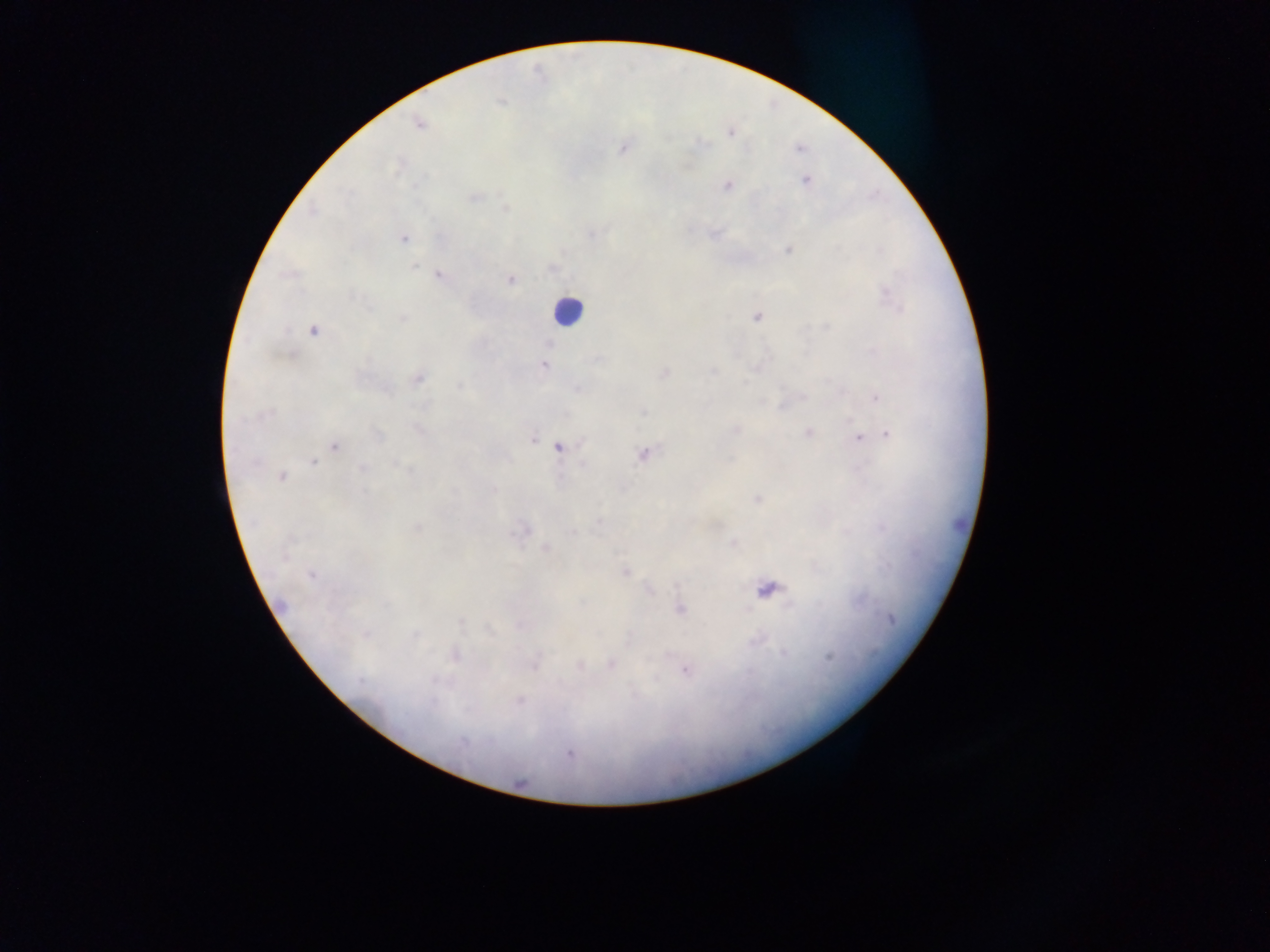
Approximate centers as [x, y] in pixels. Leukocyte locations: [567, 311]. Plasmodium parasite locations: [501, 102], [419, 124], [731, 133], [623, 148], [798, 149], [806, 181], [727, 185], [474, 197], [505, 208], [312, 212], [593, 234], [403, 238], [788, 250], [880, 250], [415, 266], [553, 269], [439, 276], [511, 280], [886, 292], [758, 317], [403, 318], [826, 327], [313, 330], [550, 343], [597, 360], [543, 366], [665, 372], [712, 372], [418, 379], [744, 382], [459, 385], [578, 389], [803, 397], [876, 398], [643, 412], [269, 413], [418, 430], [735, 430], [808, 433], [887, 434], [378, 435], [858, 437], [533, 439], [335, 446], [560, 448], [642, 454], [314, 462], [394, 464], [362, 468], [409, 470], [282, 476], [494, 489], [364, 491], [757, 499], [599, 522], [416, 528], [525, 530], [572, 532], [733, 543], [545, 548], [625, 572], [311, 575], [769, 591], [680, 609], [891, 619], [461, 622], [489, 630], [366, 634], [415, 635], [783, 653], [456, 655], [829, 657], [612, 664], [535, 665], [580, 666], [685, 670], [361, 682], [520, 700], [432, 703], [462, 742], [569, 754]. Collected in Ghana. Image is 1270×952 pixels. One field of view. Thick blood smear. Mobile-phone photograph taken through the microscope.